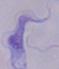 A trypanosome is shown. 1000x magnification. Micrograph.